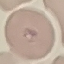

{
  "result": "malaria parasites detected",
  "capture": "smartphone through the microscope eyepiece",
  "stain": "Giemsa",
  "preparation": "thin smear",
  "image_type": "automatically extracted cell patch, resized to 64 × 64 pixels"
}